Comment on the morphology of the erythrocytes.
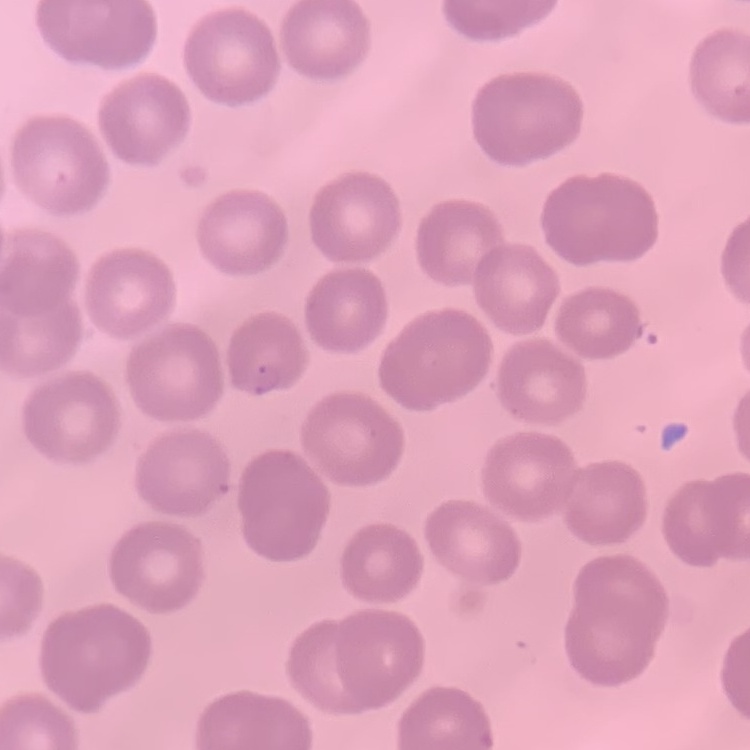
They show no rouleaux formation.

stain: Field's or Giemsa
image_type: one tile cut from a larger photomicrograph
preparation: thin peripheral smear